Identify the parasite.
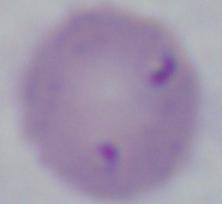
This is Babesia.

Summary:
  - Magnification: 1000x
  - Modality: micrograph